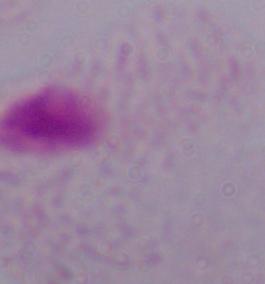 A trichomonad is shown. 1000x magnification. Micrograph.